Report the malaria status of this cell.
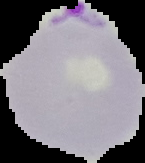
It is parasitized.

Segmented cell region on a black background. From a thin blood film. Image is 145×163 pixels.